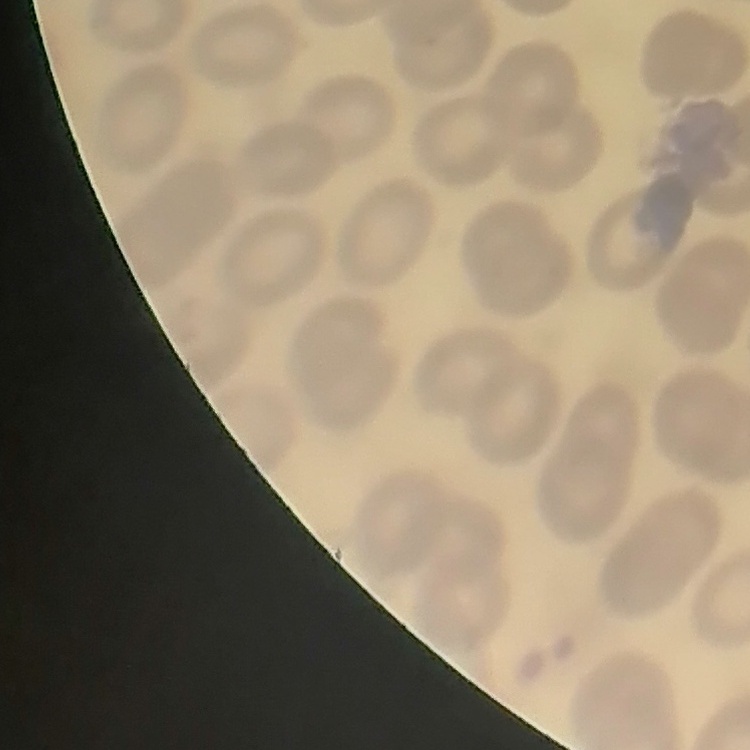

{
  "red_blood_cell_morphology": "no rouleaux formation",
  "stain": "Field's or Giemsa",
  "preparation": "thin blood smear",
  "image_type": "one tile cut from a larger photomicrograph"
}